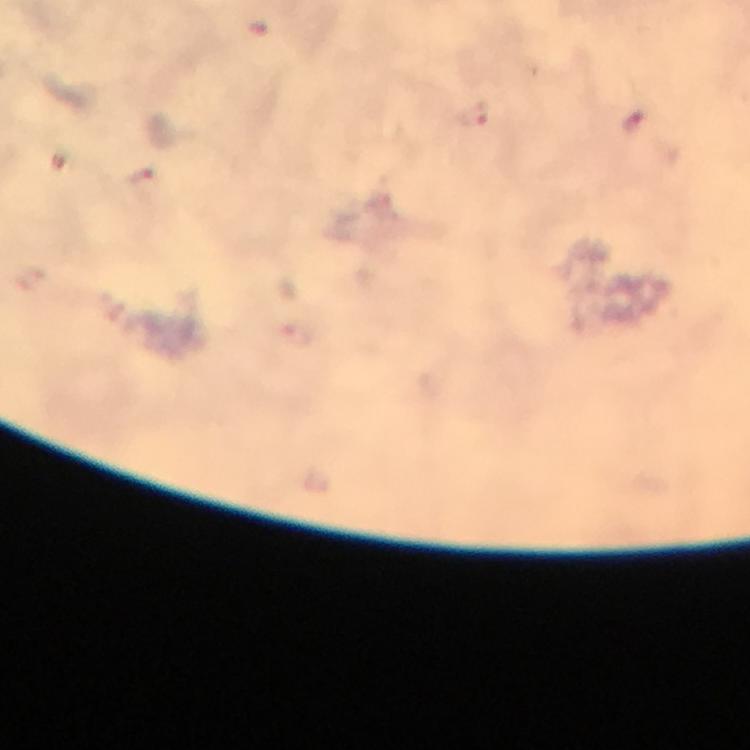

preparation: thick blood smear
image_size: 750×750 pixels
immersion_oil: applied
plasmodium_parasite_locations: 'approximate centers as (x, y) in pixels: (472, 117), (144, 183)'
context: from a diagnostic examination for malaria
cropped_from: a single field of view
magnification: 100x
capture: smartphone camera through the microscope
stain: Giemsa